Locate every Plasmodium parasite.
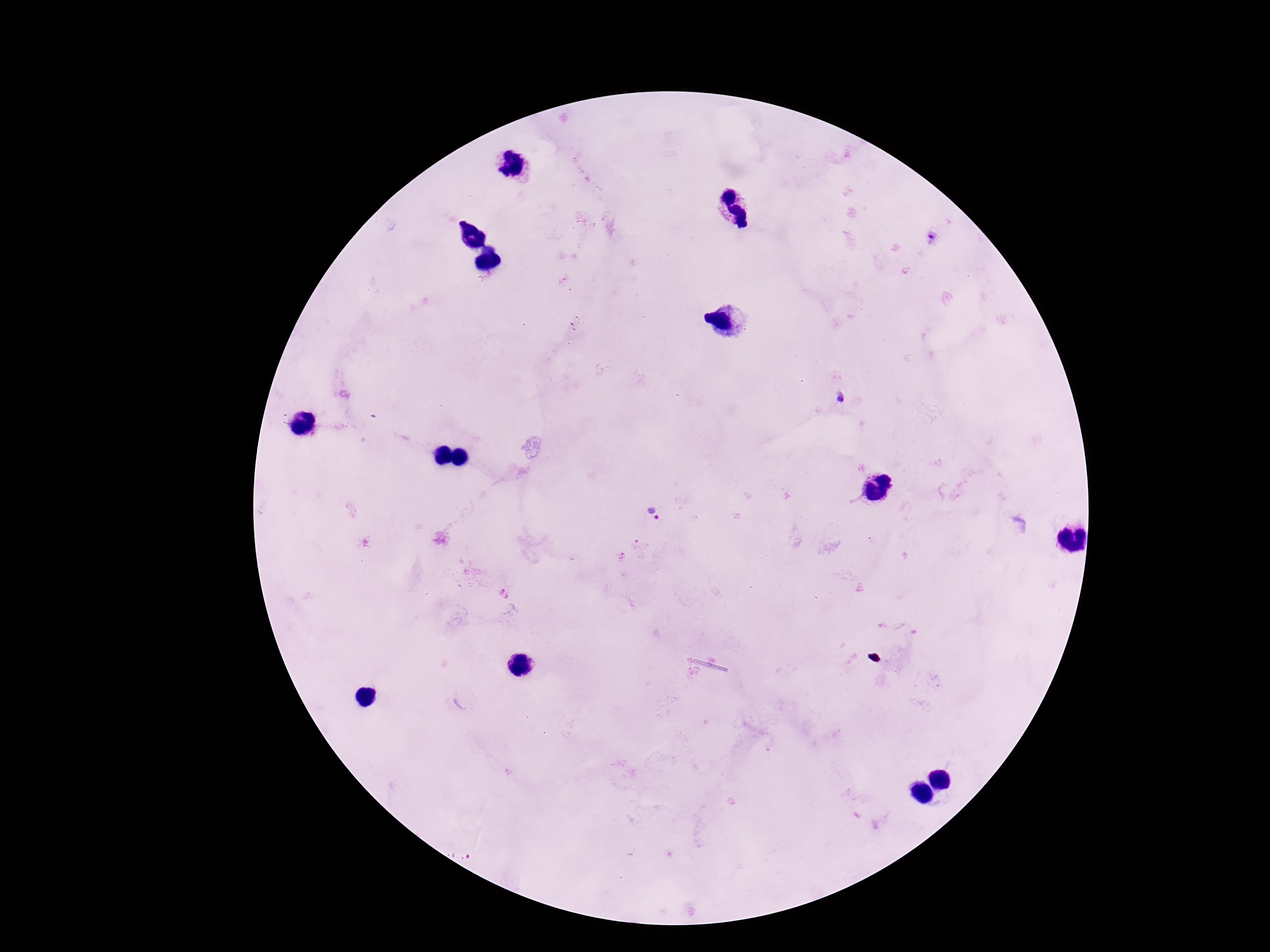
Approximate centers as (x, y) in pixels.
Plasmodium parasites: (931, 238), (839, 399), (653, 516).

capture = smartphone camera through the microscope eyepiece
field of view = single
preparation = thick blood smear
image size = 1270×952 pixels
patient malaria status = positive
stain = Giemsa
magnification = 100x